Locate every Plasmodium ovale-infected red blood cell.
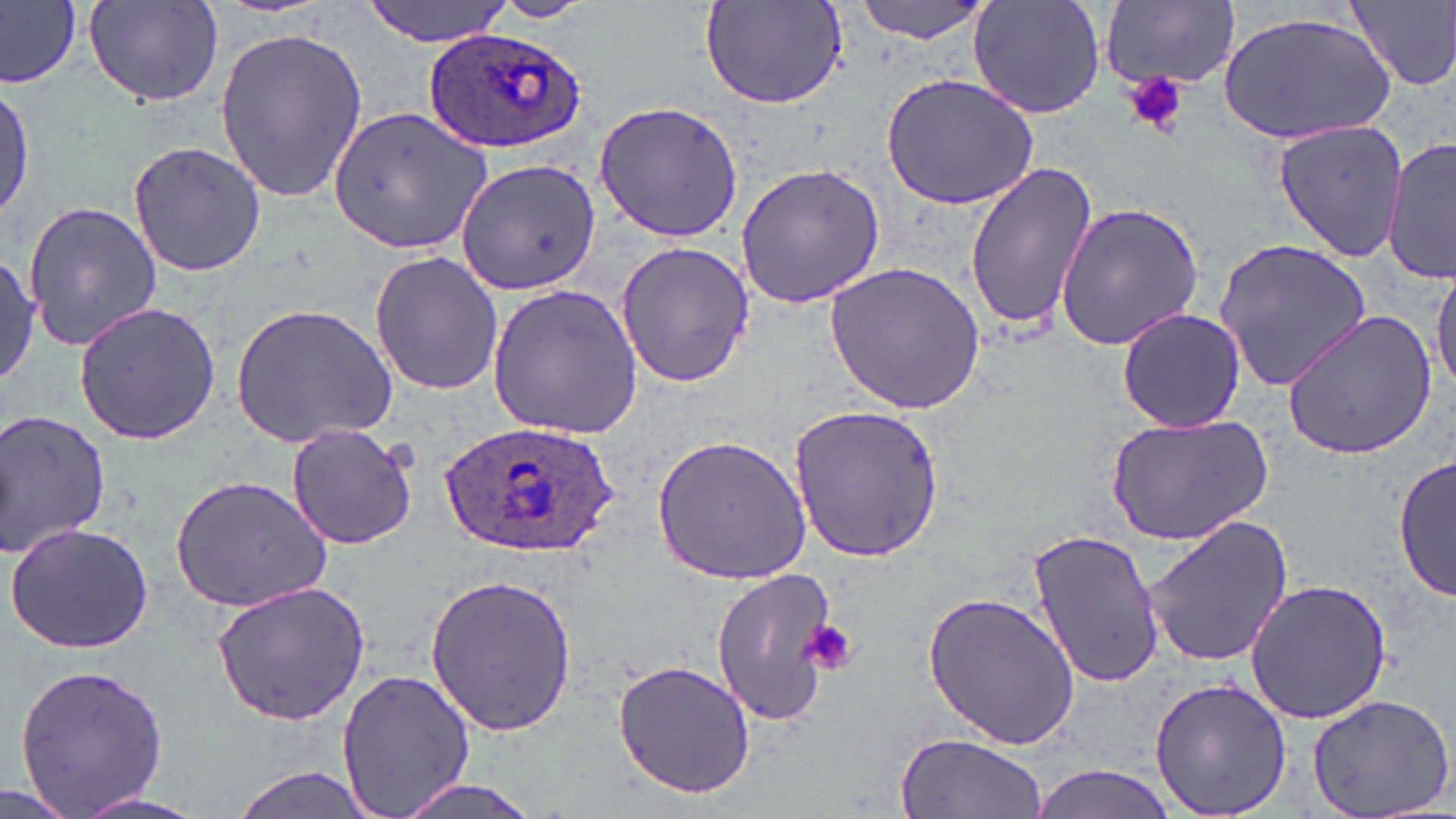

Approximate bounding boxes as (x1, y1, x2, y2) in pixels.
Plasmodium ovale-infected red blood cells: (426, 26, 588, 155), (434, 420, 622, 559).

Summary:
  - Uninfected red blood cell locations: (0, 0, 80, 90), (360, 0, 515, 46), (699, 0, 851, 111), (851, 0, 994, 43), (1349, 0, 1456, 90), (483, 1, 598, 24), (969, 1, 1104, 119), (83, 2, 225, 108), (1101, 2, 1238, 90), (1217, 10, 1396, 146), (213, 25, 369, 203), (882, 74, 1038, 209), (0, 77, 35, 224), (593, 99, 744, 241), (328, 104, 492, 255), (1272, 120, 1409, 264), (126, 140, 266, 278), (1384, 140, 1455, 286), (457, 159, 600, 294), (735, 162, 886, 309), (962, 162, 1098, 335), (23, 200, 161, 351), (1054, 200, 1205, 351), (1213, 239, 1372, 391), (615, 241, 753, 387), (370, 250, 504, 396), (0, 251, 39, 392), (823, 259, 985, 413), (1431, 262, 1456, 396), (486, 284, 643, 442), (73, 301, 221, 445), (229, 302, 399, 449), (1116, 307, 1246, 433), (1281, 310, 1437, 459), (788, 402, 946, 565), (0, 407, 110, 558), (1103, 411, 1275, 545), (286, 422, 417, 550), (651, 433, 811, 584), (1394, 450, 1454, 603), (169, 474, 333, 615), (1142, 514, 1294, 668), (4, 521, 156, 653), (1026, 527, 1166, 688), (710, 567, 841, 728), (423, 574, 581, 736), (1243, 579, 1394, 725), (210, 581, 371, 726), (921, 588, 1080, 752), (611, 658, 759, 800), (12, 661, 171, 817), (336, 667, 477, 819), (1150, 676, 1292, 819), (1305, 691, 1455, 819), (895, 731, 1048, 819), (229, 764, 380, 819), (1026, 764, 1184, 819), (387, 776, 549, 819), (2, 778, 77, 819), (67, 791, 211, 819)
  - Platelet locations: (1122, 72, 1192, 136), (800, 618, 857, 677)
  - Slide-level diagnosis: Plasmodium ovale
  - Image size: 1456×819 pixels
  - Modality: optical microscopy
  - Magnification: 1000x
  - Preparation: thin blood smear
  - Field of view: single
  - Stain: May-Grünwald-Giemsa